Assess the morphology of the erythrocytes.
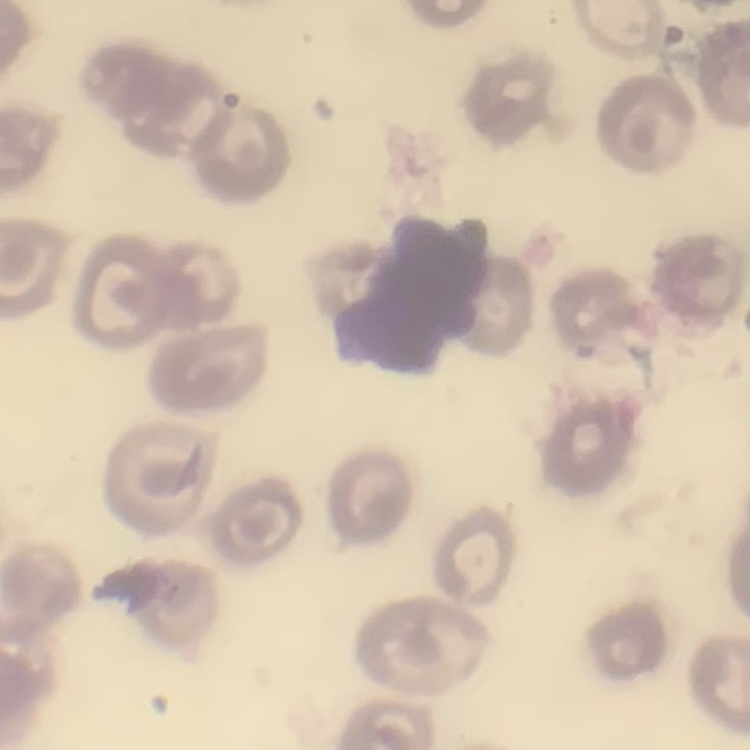

They show no rouleaux formation.

preparation = thin blood film
image type = one tile cut from a larger photomicrograph
stain = Field's or Giemsa